Assess this cell for malaria.
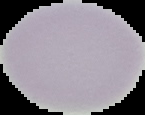
It is uninfected.

preparation: thin blood film
image_type: cell region segmented out of the field of view; surrounding area masked to black
image_size: 145×115 pixels